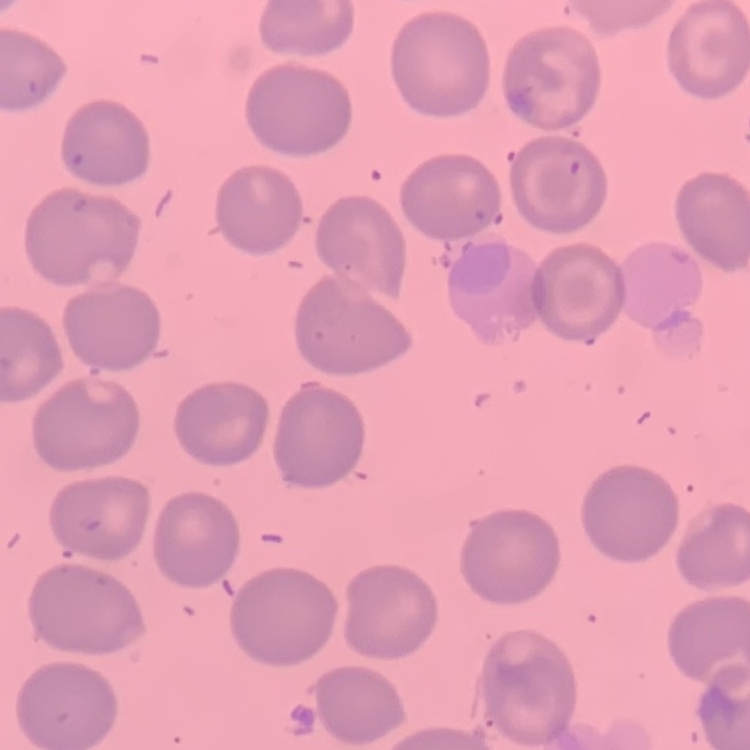 The erythrocytes exhibit no rouleaux formation. One tile cut from a larger photomicrograph. Thin blood film. Stained with either Field's or Giemsa.